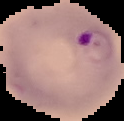
From a thin blood film. Malaria status: parasitized. Image is 124×121 pixels. Cell region segmented out of the field of view; the surrounding area is masked to black.